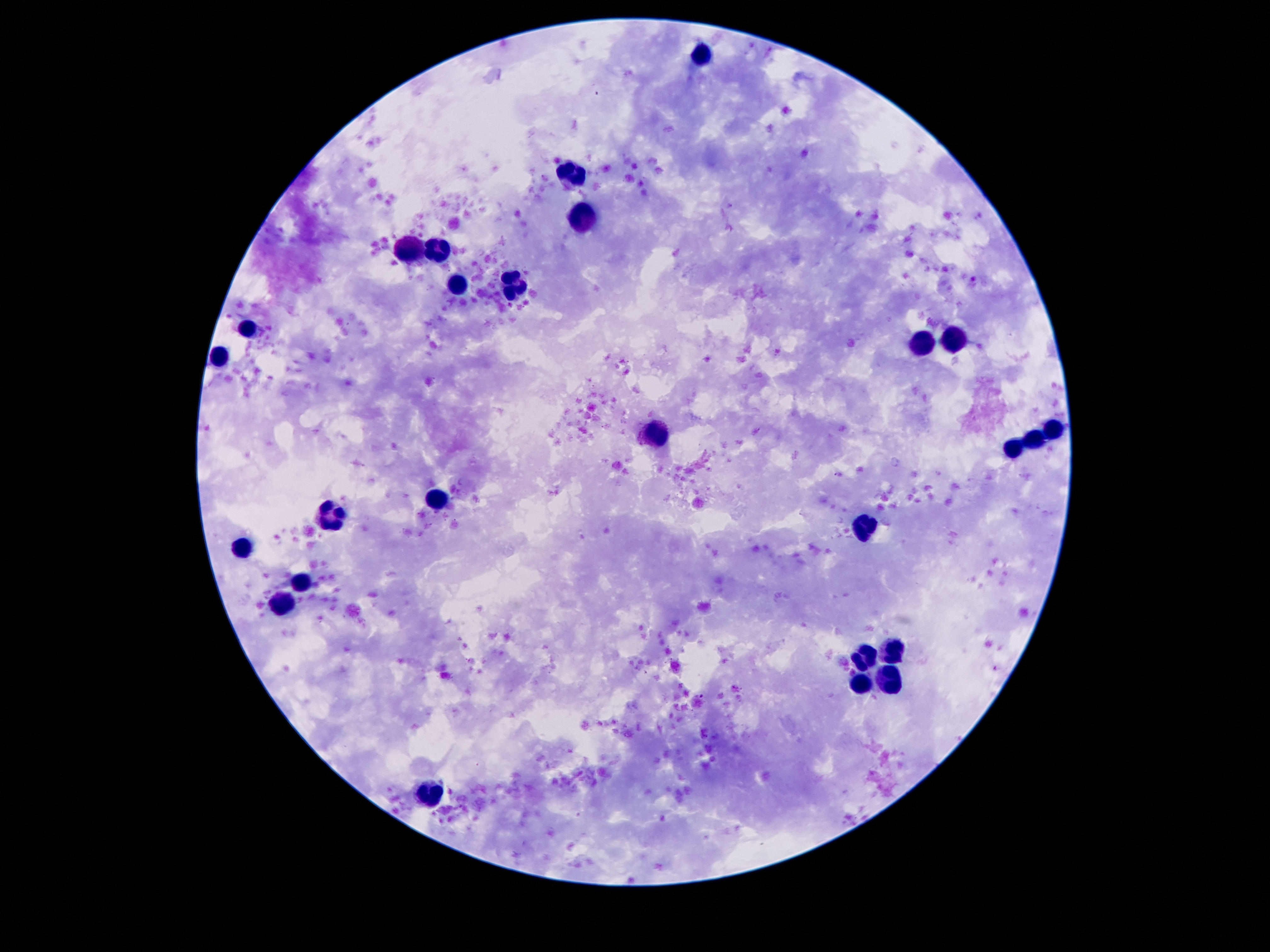
Approximate centers as {x, y} in pixels.
Summary:
  - Leukocyte locations: {704, 55}, {571, 174}, {582, 215}, {438, 246}, {412, 248}, {512, 287}, {457, 289}, {248, 330}, {956, 340}, {920, 344}, {217, 357}, {1053, 428}, {659, 432}, {1036, 439}, {1012, 451}, {438, 498}, {334, 516}, {862, 527}, {244, 545}, {305, 582}, {281, 604}, {893, 650}, {864, 658}, {885, 681}, {860, 686}, {430, 797}
  - Preparation: thick blood smear
  - Capture: smartphone camera through the microscope eyepiece
  - Magnification: 100x
  - Image size: 1270×952 pixels
  - Stain: Giemsa
  - Patient malaria status: not infected
  - Field of view: single